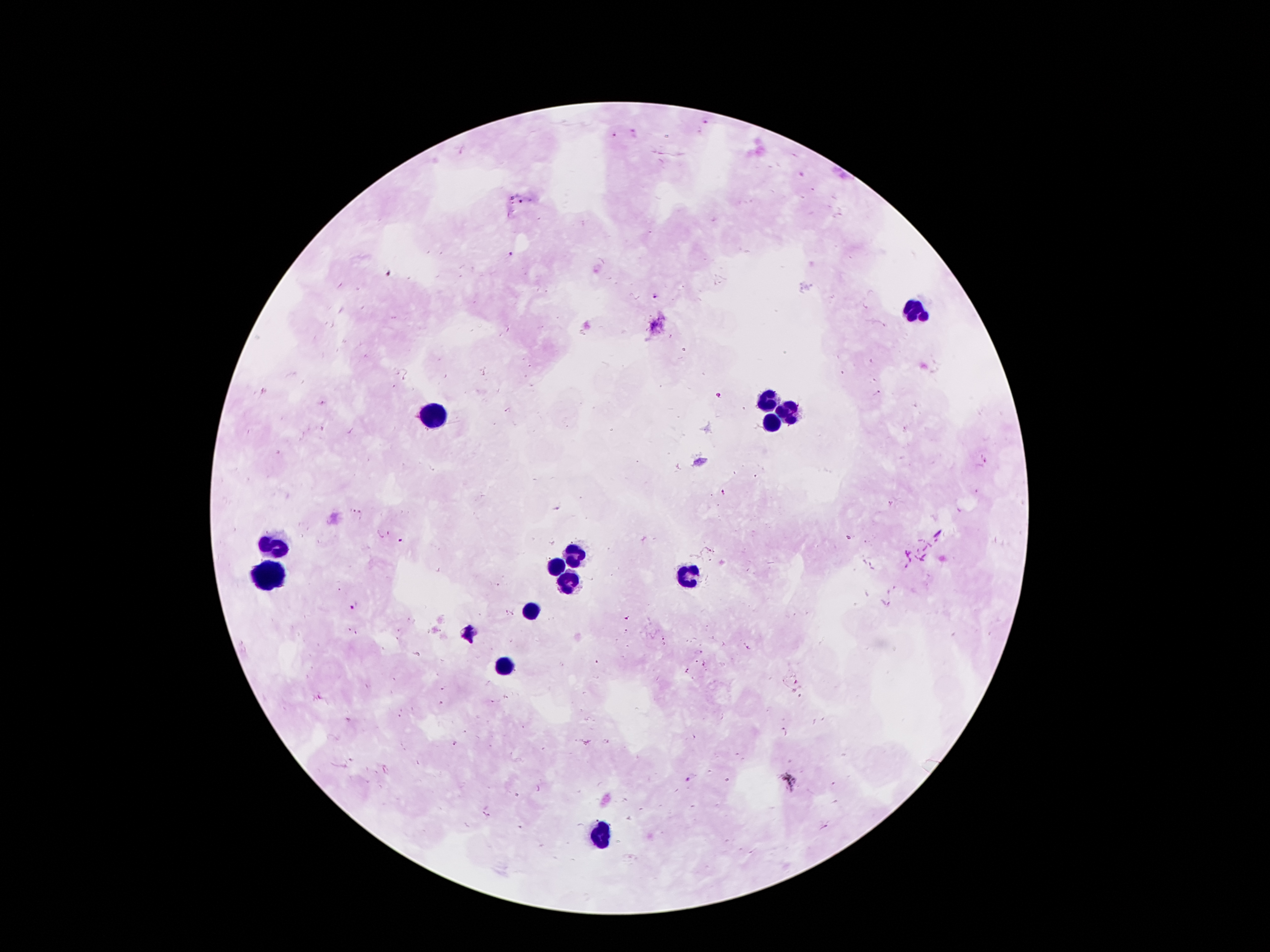

{
  "image_size": "1270×952 pixels",
  "capture": "smartphone through the microscope eyepiece",
  "malaria_parasite_locations": "approximate centers as [x, y] in pixels: [705, 119], [612, 136], [522, 200], [511, 254], [655, 297], [878, 392], [323, 403], [558, 508], [356, 513], [401, 542], [354, 605], [471, 634], [321, 696], [493, 701], [441, 702], [606, 741], [583, 743], [455, 744], [688, 780], [489, 815]",
  "leukocyte_locations": "approximate centers as [x, y] in pixels: [918, 315], [770, 399], [431, 415], [786, 415], [766, 421], [273, 543], [575, 553], [553, 567], [688, 575], [267, 577], [565, 579], [531, 611], [505, 664], [599, 838]",
  "field_of_view": "one from this slide",
  "patient_malaria_status": "infected with Plasmodium falciparum",
  "magnification": "100x",
  "preparation": "thick blood film",
  "stain": "Giemsa"
}